Classify this cell by malaria status.
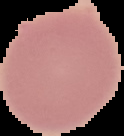

It is uninfected.

Summary:
  - Preparation: thin blood film
  - Image type: cell region segmented out of the field of view; surrounding area masked to black
  - Image size: 124×136 pixels